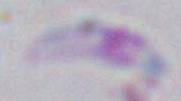

Micrograph. Toxoplasma gondii is seen. Captured at 1000x magnification.